State which parasite is depicted.
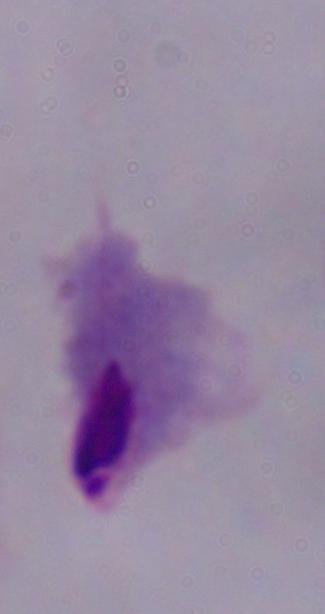
A trichomonad.

magnification = 1000x
modality = micrograph